Identify the cell.
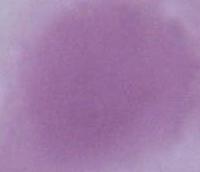

This is an erythrocyte.

Summary:
  - Modality: micrograph
  - Magnification: 1000x